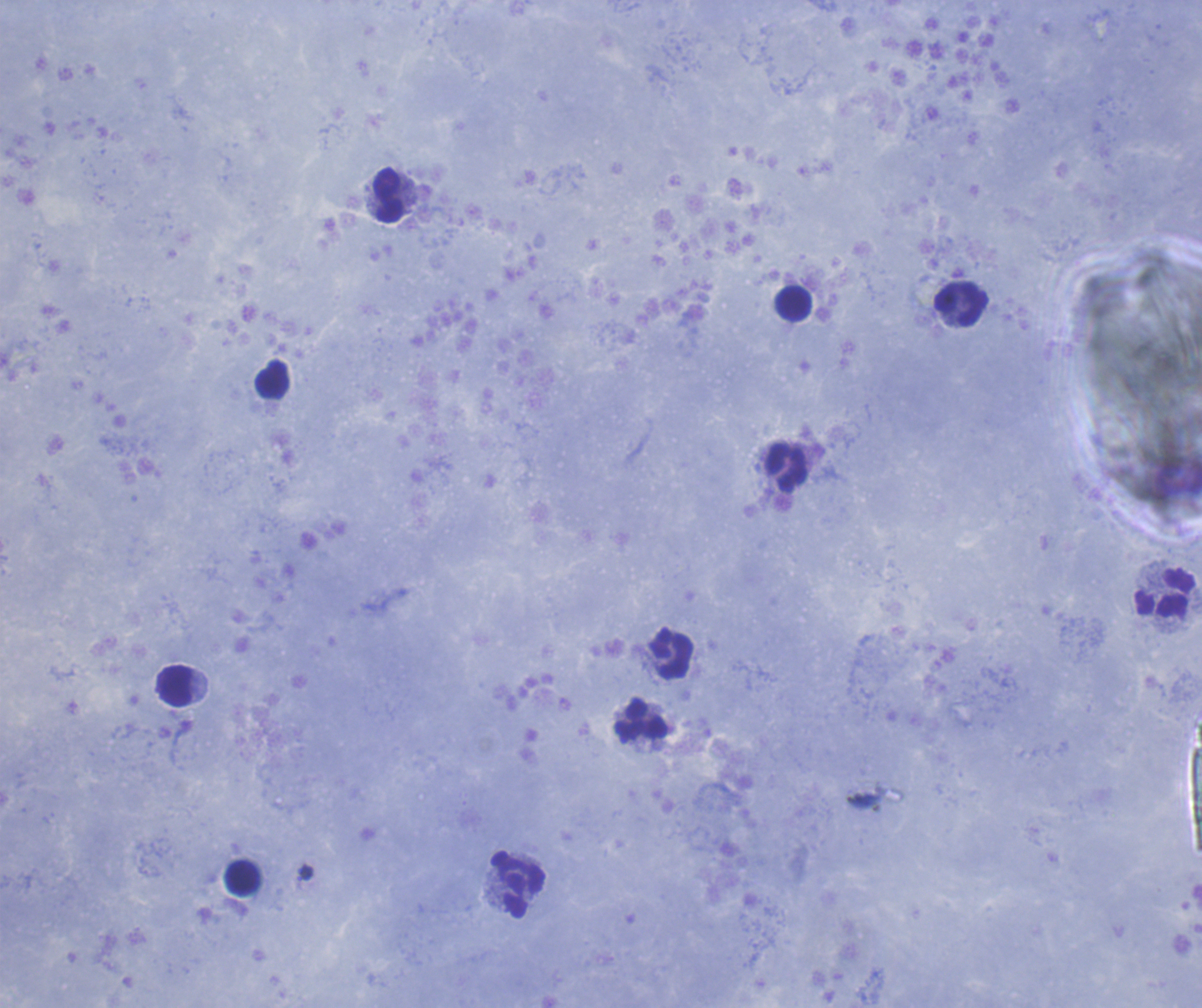 Approximate centers as {x, y} in pixels. Leukocyte locations: {388, 194}, {794, 304}, {961, 304}, {272, 379}, {786, 468}, {1164, 593}, {670, 653}, {174, 686}, {640, 721}, {243, 878}, {517, 884}. Captured at 100x magnification. Result: negative for Plasmodium parasites. Single field of view. Previously used in a real diagnosis. Background quality: good. Thick blood film. Coloration quality: good. Image is 1202×1008 pixels. Romanowsky stain.